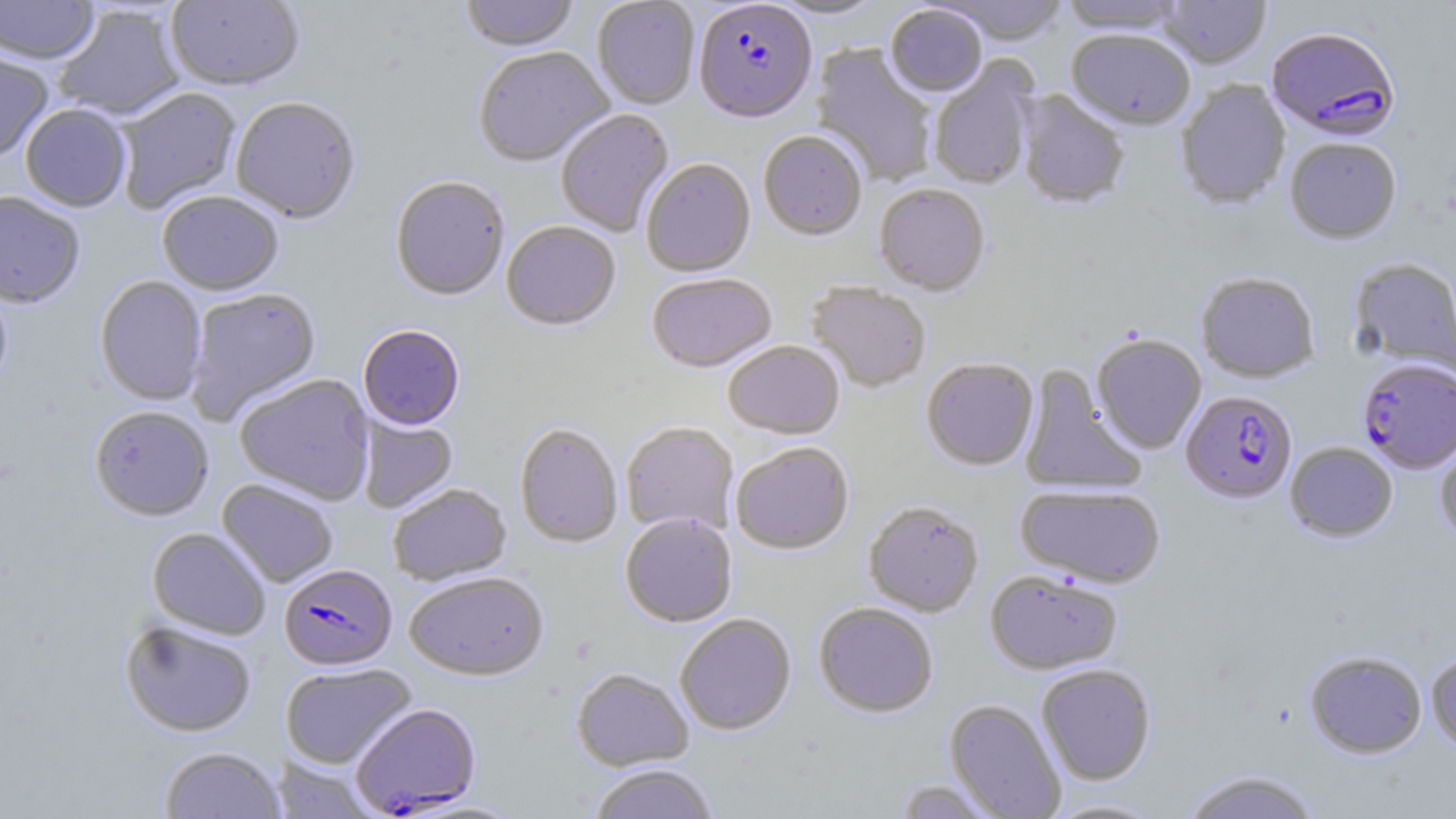

slide-level diagnosis = Plasmodium falciparum
preparation = thin blood smear
modality = light microscopy
uninfected red blood cell locations = approximate bounding boxes as named x1/y1/x2/y2 corners in pixels: (x1=0, y1=0, x2=99, y2=66), (x1=166, y1=0, x2=304, y2=93), (x1=459, y1=0, x2=580, y2=54), (x1=770, y1=0, x2=887, y2=21), (x1=930, y1=0, x2=1072, y2=47), (x1=1058, y1=0, x2=1189, y2=35), (x1=1158, y1=0, x2=1271, y2=69), (x1=592, y1=1, x2=700, y2=110), (x1=52, y1=4, x2=186, y2=121), (x1=885, y1=5, x2=988, y2=98), (x1=1066, y1=30, x2=1195, y2=132), (x1=810, y1=43, x2=938, y2=188), (x1=0, y1=46, x2=54, y2=162), (x1=473, y1=49, x2=615, y2=168), (x1=928, y1=57, x2=1039, y2=191), (x1=1176, y1=80, x2=1291, y2=210), (x1=114, y1=87, x2=242, y2=214), (x1=1015, y1=89, x2=1130, y2=210), (x1=230, y1=98, x2=361, y2=225), (x1=20, y1=104, x2=132, y2=213), (x1=555, y1=109, x2=674, y2=237), (x1=758, y1=132, x2=867, y2=242), (x1=1284, y1=138, x2=1402, y2=246), (x1=641, y1=160, x2=756, y2=278), (x1=390, y1=177, x2=510, y2=302), (x1=875, y1=184, x2=990, y2=297), (x1=0, y1=192, x2=86, y2=309), (x1=157, y1=192, x2=283, y2=296), (x1=501, y1=222, x2=621, y2=332), (x1=1349, y1=257, x2=1456, y2=376), (x1=1196, y1=272, x2=1320, y2=383), (x1=646, y1=273, x2=777, y2=374), (x1=94, y1=276, x2=207, y2=405), (x1=0, y1=281, x2=13, y2=397), (x1=806, y1=282, x2=932, y2=393), (x1=185, y1=287, x2=321, y2=425), (x1=358, y1=325, x2=465, y2=431), (x1=1091, y1=334, x2=1207, y2=454), (x1=723, y1=341, x2=844, y2=440), (x1=921, y1=358, x2=1038, y2=471), (x1=1018, y1=364, x2=1146, y2=496), (x1=233, y1=373, x2=376, y2=505), (x1=90, y1=405, x2=214, y2=521), (x1=357, y1=416, x2=458, y2=513), (x1=621, y1=421, x2=739, y2=537), (x1=514, y1=423, x2=623, y2=548), (x1=1434, y1=432, x2=1456, y2=550), (x1=730, y1=442, x2=854, y2=556), (x1=1285, y1=442, x2=1398, y2=543), (x1=218, y1=479, x2=338, y2=588), (x1=1015, y1=483, x2=1166, y2=589), (x1=388, y1=484, x2=511, y2=586), (x1=863, y1=501, x2=984, y2=617), (x1=620, y1=513, x2=737, y2=627), (x1=147, y1=527, x2=271, y2=640), (x1=985, y1=570, x2=1123, y2=675), (x1=405, y1=572, x2=548, y2=681), (x1=814, y1=602, x2=939, y2=718), (x1=675, y1=613, x2=797, y2=735), (x1=120, y1=620, x2=256, y2=737), (x1=1305, y1=650, x2=1427, y2=759), (x1=1426, y1=650, x2=1456, y2=756), (x1=280, y1=663, x2=416, y2=769), (x1=1036, y1=663, x2=1157, y2=785), (x1=571, y1=667, x2=694, y2=772), (x1=944, y1=699, x2=1067, y2=819), (x1=159, y1=746, x2=285, y2=819), (x1=272, y1=756, x2=380, y2=819), (x1=589, y1=764, x2=720, y2=818), (x1=1180, y1=769, x2=1324, y2=819), (x1=893, y1=778, x2=1004, y2=818), (x1=1041, y1=797, x2=1171, y2=818)
image size = 1456×819 pixels
magnification = 1000x
Plasmodium falciparum-infected red blood cell locations = approximate bounding boxes as named x1/y1/x2/y2 corners in pixels: (x1=694, y1=3, x2=817, y2=126), (x1=1266, y1=27, x2=1400, y2=143), (x1=1357, y1=358, x2=1456, y2=474), (x1=1181, y1=391, x2=1298, y2=505), (x1=280, y1=563, x2=397, y2=671), (x1=351, y1=703, x2=483, y2=815)
field of view = single
stain = May-Grünwald-Giemsa